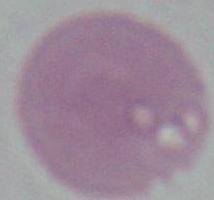

identification = red blood cell
modality = photomicrograph
magnification = 1000x